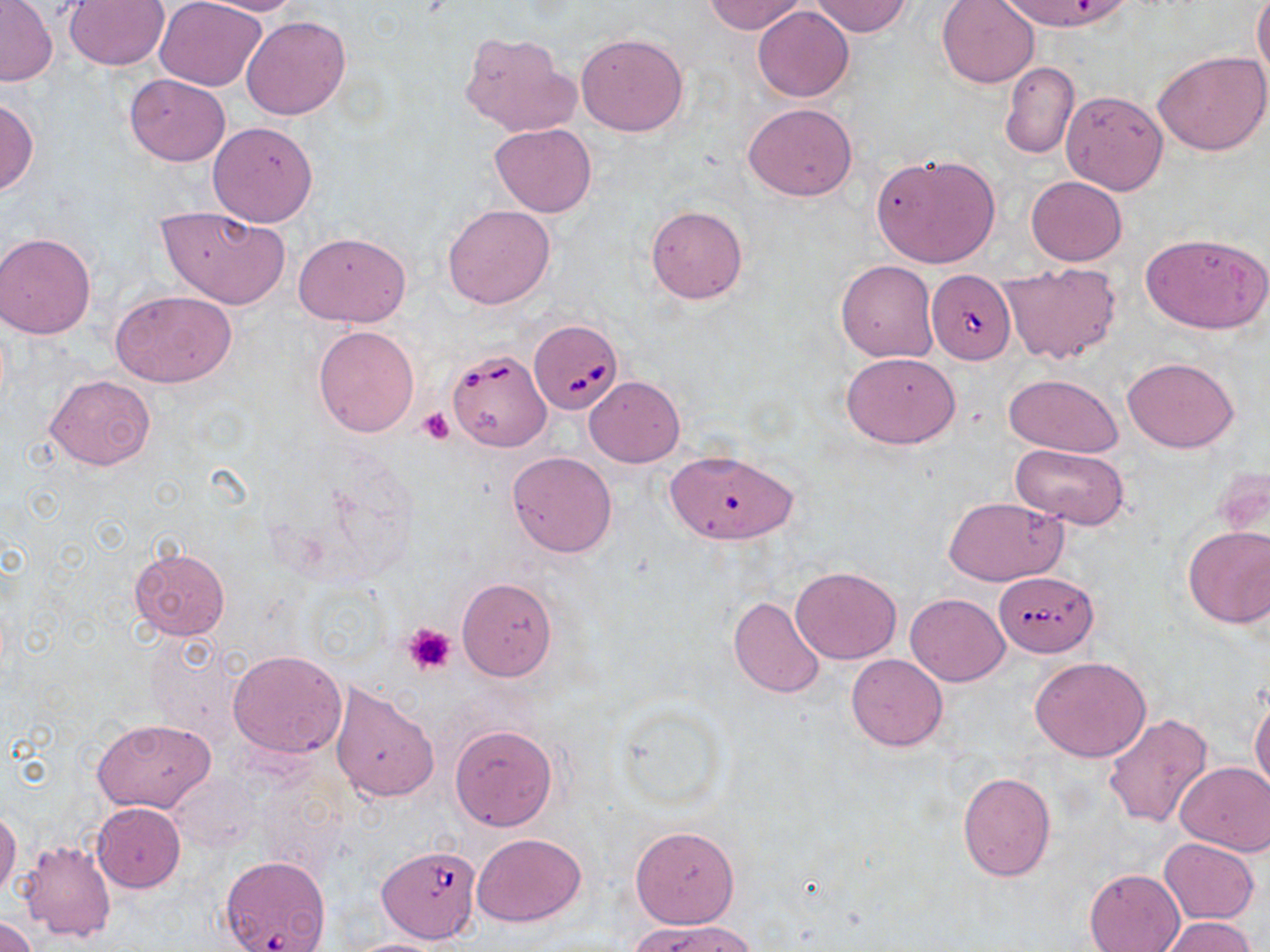
Approximate bounding boxes as (x1, y1, x2, y2) in pixels. Uninfected red blood cell locations: (64, 0, 170, 70), (154, 0, 267, 90), (188, 0, 309, 16), (703, 0, 809, 34), (938, 0, 1039, 87), (1000, 0, 1133, 33), (1, 1, 57, 86), (808, 1, 912, 37), (1253, 1, 1270, 85), (753, 5, 854, 101), (241, 15, 350, 121), (577, 32, 688, 136), (459, 33, 579, 137), (1154, 50, 1270, 156), (999, 60, 1079, 159), (125, 73, 230, 166), (1061, 91, 1168, 194), (0, 95, 38, 195), (744, 103, 857, 201), (207, 121, 317, 226), (489, 123, 597, 218), (872, 152, 1000, 267), (1025, 176, 1127, 265), (442, 204, 555, 310), (158, 205, 289, 308), (646, 206, 748, 302), (1, 232, 96, 338), (294, 232, 411, 327), (1140, 232, 1270, 334), (998, 260, 1122, 365), (836, 261, 938, 362), (110, 291, 236, 388), (313, 324, 420, 437), (842, 352, 959, 449), (1122, 357, 1239, 453), (1005, 372, 1123, 456), (44, 374, 156, 471), (585, 376, 684, 468), (1010, 443, 1129, 530), (663, 449, 799, 545), (507, 451, 617, 557), (943, 496, 1068, 585), (1182, 525, 1270, 628), (128, 545, 230, 641), (790, 566, 902, 664), (457, 576, 558, 681), (905, 592, 1010, 686), (728, 595, 826, 699), (228, 648, 347, 759), (845, 653, 949, 751), (1030, 657, 1150, 762), (329, 681, 440, 803), (1249, 689, 1270, 797), (1103, 712, 1213, 829), (92, 716, 216, 812), (449, 724, 557, 832), (1176, 761, 1270, 856), (168, 770, 262, 854), (957, 770, 1056, 882), (92, 802, 185, 892), (0, 809, 21, 900), (630, 825, 740, 927), (471, 832, 586, 927), (1159, 838, 1260, 924), (19, 840, 116, 941), (1084, 868, 1185, 952), (0, 914, 40, 951), (1159, 917, 1258, 951), (632, 918, 758, 952), (337, 937, 453, 952). Babesia divergens-infected red blood cell locations: (926, 270, 1014, 364), (529, 317, 627, 415), (446, 347, 553, 452), (995, 570, 1097, 655), (377, 845, 481, 945), (219, 855, 330, 950). Platelet locations: (417, 407, 453, 444), (403, 622, 457, 675). Slide-level diagnosis: Babesia divergens. May-Grünwald-Giemsa-stained preparation. Single field of view. Captured at 1000x magnification. Image is 1270×952 pixels. Thin blood smear. Optical microscopy.